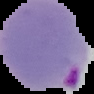 Image is 94×94 pixels. Segmented cell region on a black background. From a thin blood film. Result: malaria parasites detected.